Assess this cell for malaria.
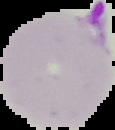

It is parasitized.

From a thin blood film. Image is 115×130 pixels. Segmented cell region on a black background.